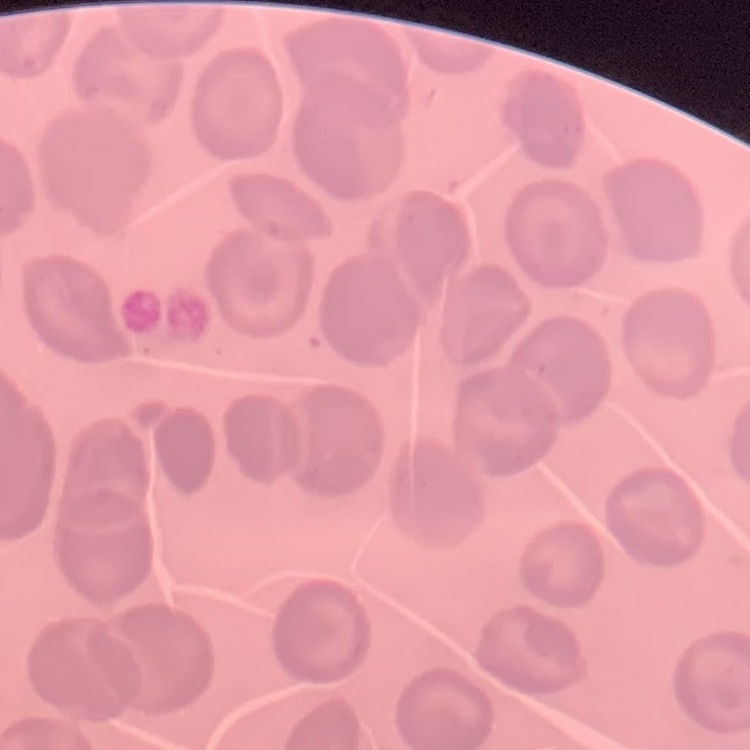
The erythrocytes exhibit no rouleaux formation. Stained with either Field's or Giemsa. One tile cut from a larger photomicrograph. Thin peripheral smear.